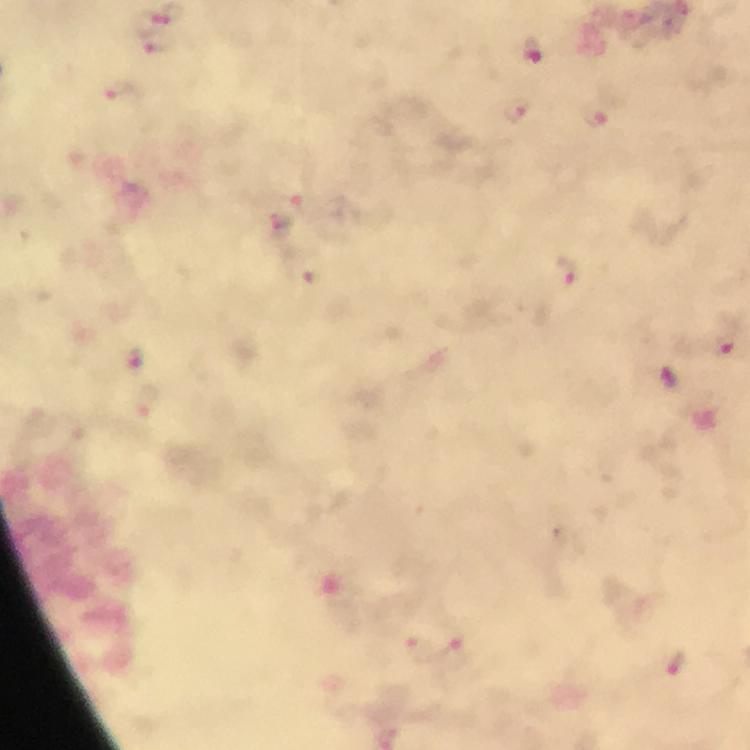
Approximate centers as [x, y] in pixels.
Summary:
  - Plasmodium parasite locations: [166, 13], [532, 49], [121, 96], [518, 108], [595, 119], [281, 222], [568, 268], [312, 278], [727, 345], [135, 356], [670, 379], [676, 663]
  - Context: from a malaria diagnostic workup
  - Image size: 750×750 pixels
  - Immersion oil: used
  - Preparation: thick smear
  - Cropped from: a single field of view
  - Capture: smartphone mounted on the microscope
  - Stain: Giemsa
  - Magnification: 100x